Assess for malaria.
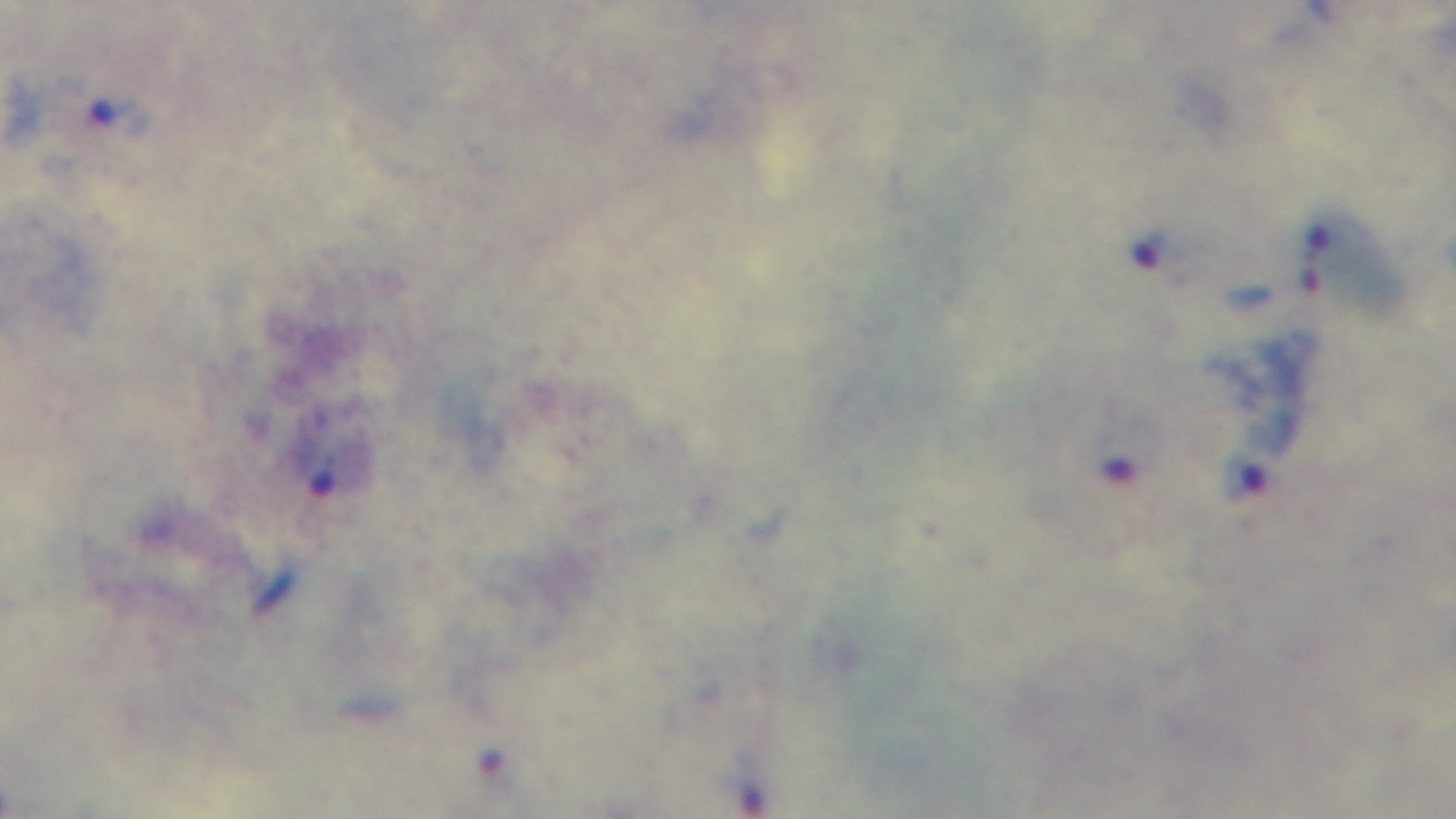

Infected.

Summary:
  - Preparation: thick blood film
  - Objective: 100x oil immersion
  - Stain: Giemsa
  - Modality: light microscopy
  - Capture: mounted 4K digital camera
  - Field of view: one from the slide